State which parasite is depicted.
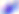

This is Toxoplasma gondii.

Summary:
  - Magnification: 400x
  - Modality: photomicrograph